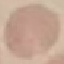

result = negative for malaria parasites
image type = automatically extracted cell patch, resized to 64 × 64 pixels
stain = Giemsa
preparation = thin blood smear
capture = smartphone camera at the microscope eyepiece